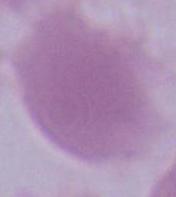
modality = photomicrograph
magnification = 1000x
identification = erythrocyte